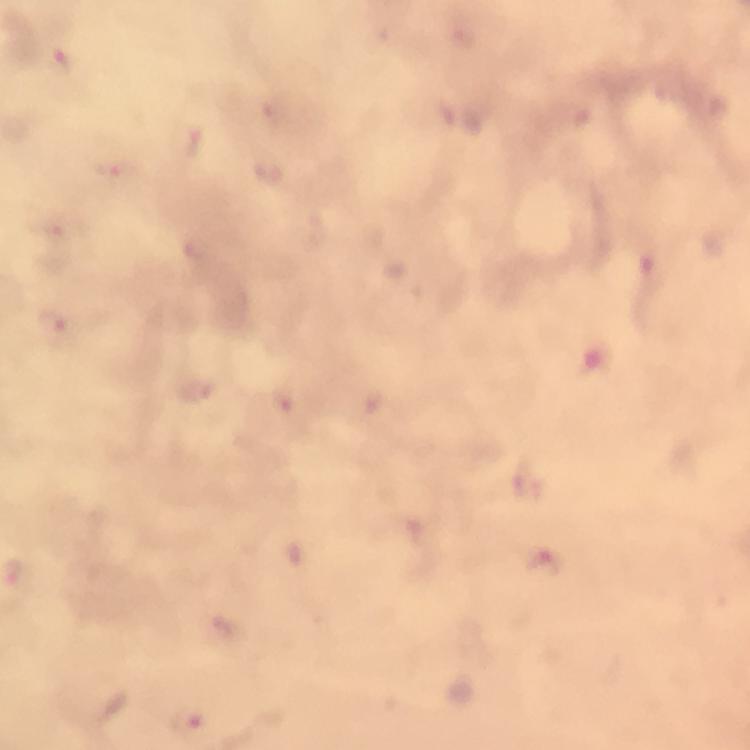
Approximate object centers, in pixels from the top-left corner.
Summary:
  - Plasmodium parasite locations: (x=195, y=143), (x=118, y=170), (x=55, y=229), (x=56, y=325), (x=289, y=401), (x=531, y=489), (x=546, y=565), (x=18, y=571), (x=230, y=633), (x=191, y=719)
  - Context: from a diagnostic examination for malaria
  - Image size: 750×750 pixels
  - Capture: smartphone mounted on the microscope
  - Stain: Giemsa
  - Preparation: thick smear
  - Cropped from: one field of view
  - Magnification: 100x
  - Immersion oil: applied